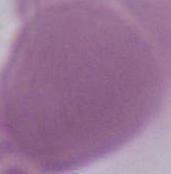

An erythrocyte is shown. Captured at 1000x magnification. Photomicrograph.